Name the parasite shown.
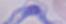

This is a trypanosome.

Captured at 1000x magnification. Micrograph.